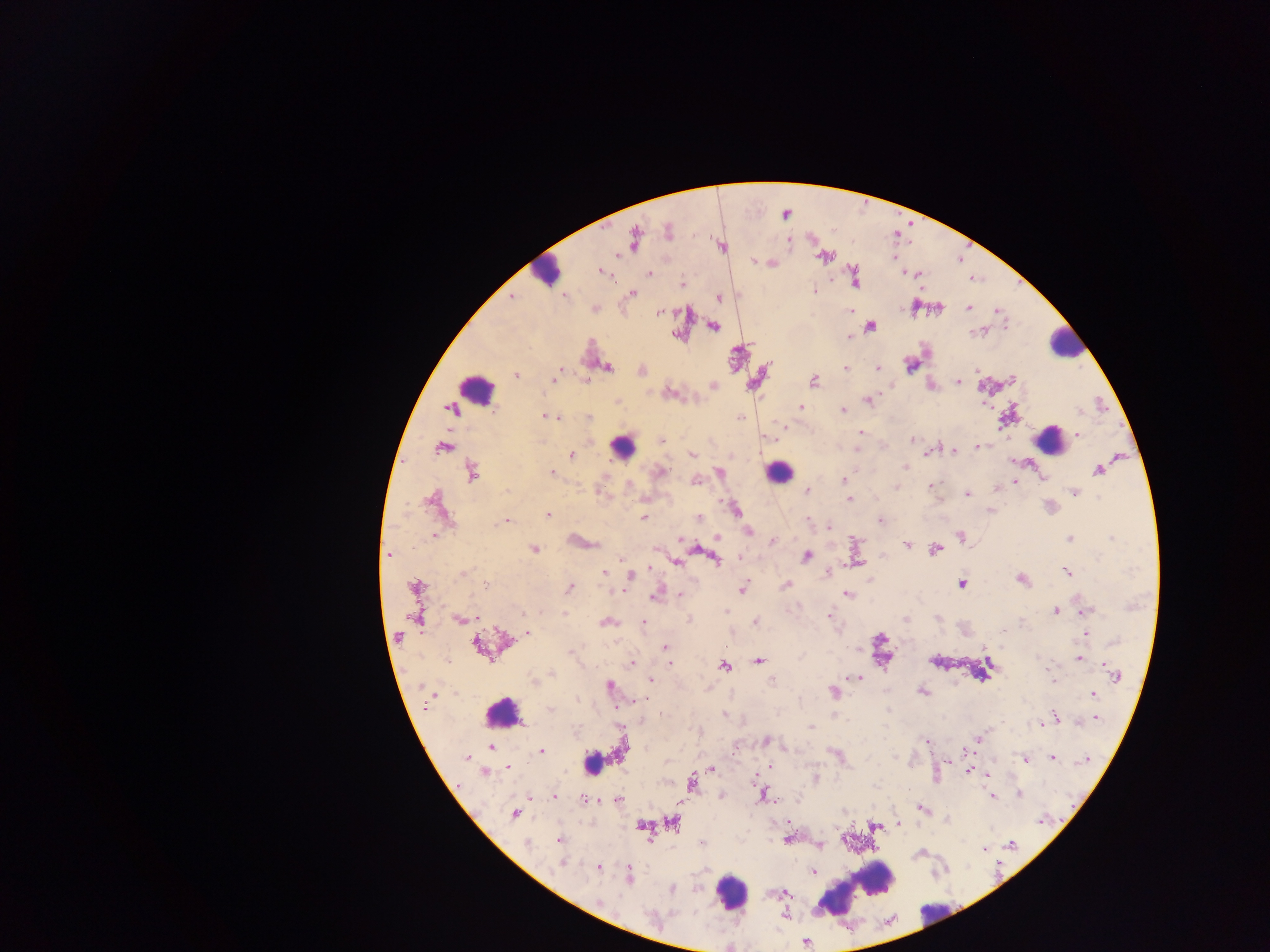
Approximate centers as x y in pixels. Leukocyte locations: 547 271; 1066 342; 475 390; 1049 439; 621 446; 778 471; 881 648; 503 712; 591 757; 866 877; 875 878; 731 893; 830 899; 935 913. Malaria parasite locations: 785 214; 668 231; 633 237; 789 241; 721 245; 824 256; 754 261; 773 263; 602 271; 903 273; 908 273; 917 273; 649 274; 854 277; 682 284; 814 291; 632 292; 510 296; 564 296; 718 297; 915 307; 594 308; 939 308; 968 308; 658 311; 850 311; 997 312; 713 325; 870 325; 981 330; 849 336; 910 364; 606 366; 845 369; 877 369; 559 370; 641 370; 975 370; 515 375; 554 376; 1011 379; 813 381; 958 381; 888 384; 931 384; 712 385; 668 393; 868 400; 985 405; 800 407; 451 409; 843 409; 548 416; 555 416; 560 417; 588 417; 741 417; 784 425; 860 432; 1078 434; 660 439; 912 439; 443 447; 978 447; 953 450; 928 451; 691 454; 571 455; 905 465; 1099 470; 471 472; 659 472; 550 473; 718 473; 1043 477; 695 480; 844 480; 1013 481; 930 486; 895 487; 995 488; 806 491; 1074 492; 847 494; 967 494; 643 497; 849 498; 433 500; 734 509; 990 510; 548 515; 641 517; 698 519; 505 520; 807 520; 880 520; 828 524; 749 531; 433 534; 961 536; 715 537; 679 538; 1068 538; 579 541; 772 541; 905 544; 533 549; 655 549; 695 549; 935 549; 388 554; 806 555; 740 557; 715 558; 622 559; 676 562; 1066 571; 827 572; 462 573; 604 574; 630 576; 1021 578; 870 581; 961 583; 486 585; 786 585; 415 587; 568 587; 619 589; 742 589; 845 593; 656 594; 680 594; 1056 610; 724 612; 1082 612; 564 613; 829 614; 414 617; 477 617; 458 618; 905 619; 606 621; 643 622; 755 622; 1084 632; 527 633; 489 646; 664 647; 1078 658; 447 660; 757 661; 1102 662; 630 663; 671 663; 724 666; 551 672; 1116 675; 857 677; 650 680; 533 681; 608 685; 922 691; 833 692; 1092 694; 550 709; 724 715; 1054 717; 1094 718; 1042 723; 810 726; 699 732; 978 738; 925 740; 765 741; 490 748; 541 751; 1052 756; 465 758; 949 760; 1026 760; 1084 760; 770 766; 507 767; 711 769; 968 770; 484 772; 987 774; 815 779; 691 783; 1019 793; 763 794; 992 795; 553 796; 528 797; 722 797; 583 799; 617 799; 920 808; 514 814; 948 820; 672 821; 787 822; 898 823; 641 825; 875 825; 787 839; 559 840; 701 843; 528 844; 819 844; 1011 844; 983 848; 919 853; 562 861; 597 867; 812 870; 628 875; 671 889; 782 893; 598 903; 784 915; 803 941. Image is 1270×952 pixels. Single field of view. Collected in Ghana. Mobile-phone photograph taken through the microscope. Thick blood film.